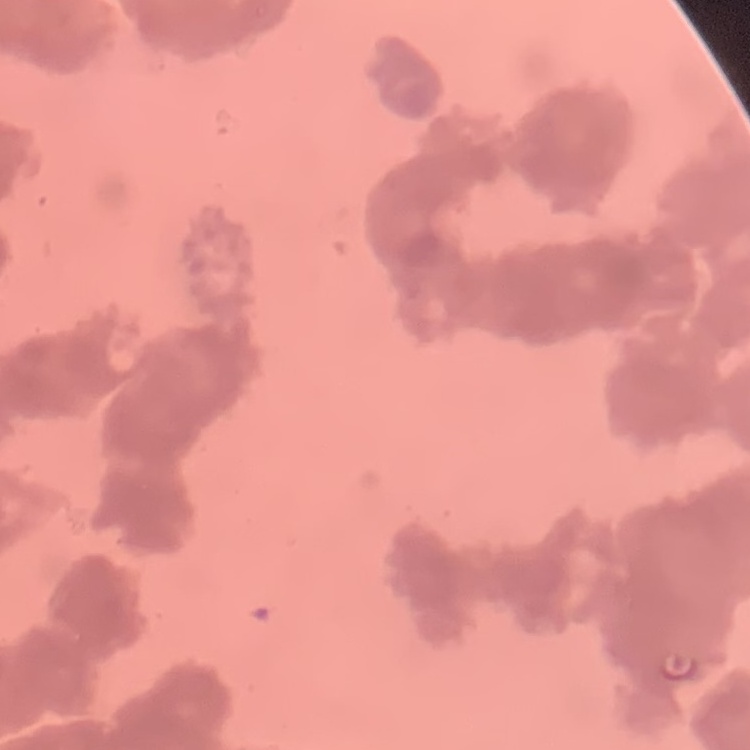

{
  "red_blood_cell_morphology": "rouleaux formation",
  "stain": "Field's or Giemsa",
  "image_type": "one tile cut from a larger photomicrograph",
  "preparation": "thin blood smear"
}